Name the parasite shown.
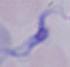
This is a trypanosome.

Summary:
  - Modality: micrograph
  - Magnification: 1000x